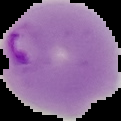

Summary:
  - Result: Plasmodium parasites identified
  - Image size: 121×121 pixels
  - Preparation: thin blood film
  - Image type: segmented cell region with the area outside set to black